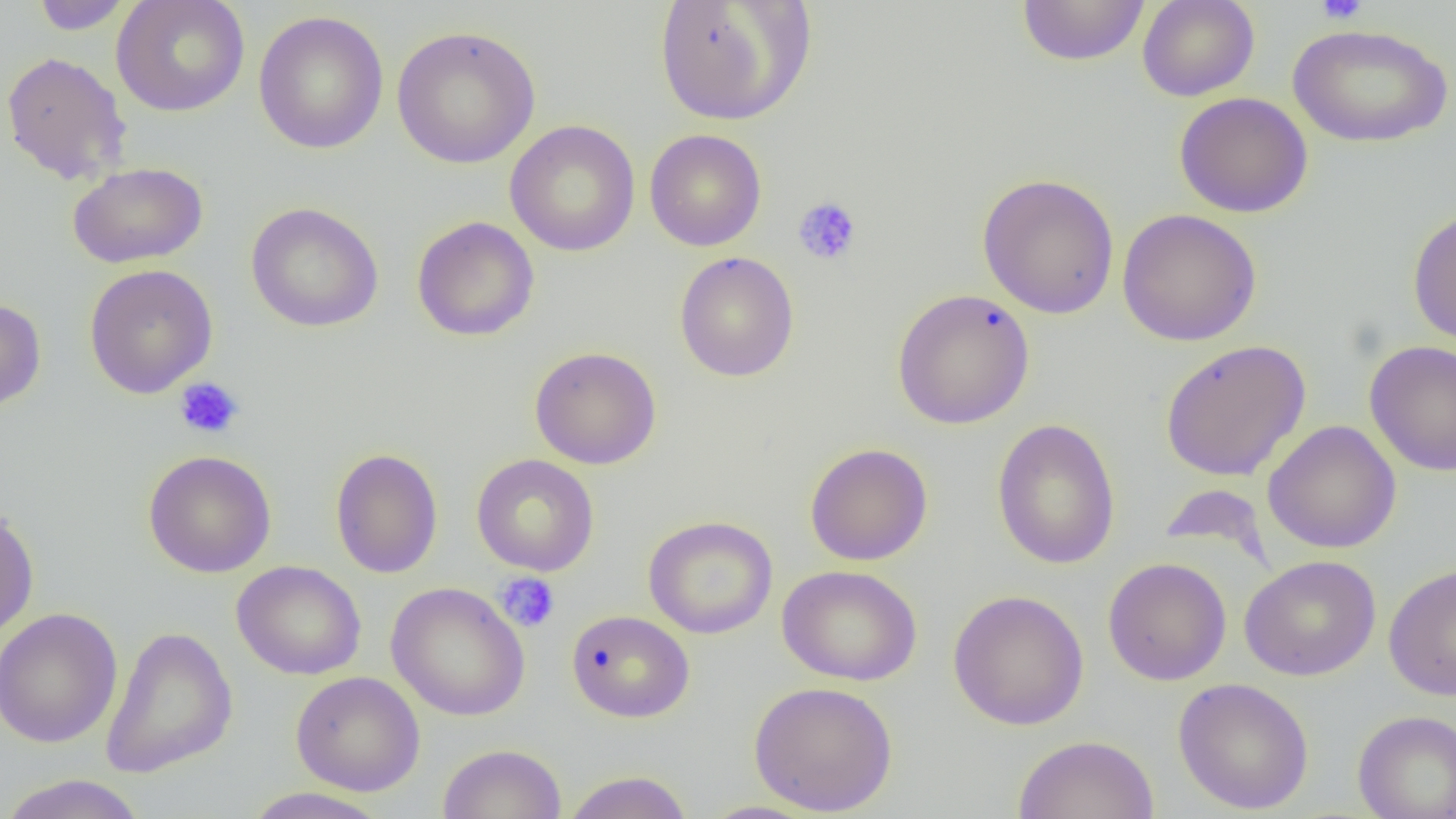

slide-level diagnosis = negative for blood parasites
image size = 1456×819 pixels
platelet locations = approximate bounding boxes as named x1/y1/x2/y2 corners in pixels: (x1=1316, y1=0, x2=1368, y2=25), (x1=793, y1=196, x2=862, y2=265), (x1=174, y1=377, x2=245, y2=440), (x1=495, y1=572, x2=560, y2=633)
uninfected red blood cell locations = approximate bounding boxes as named x1/y1/x2/y2 corners in pixels: (x1=30, y1=0, x2=133, y2=34), (x1=110, y1=0, x2=250, y2=117), (x1=653, y1=0, x2=816, y2=127), (x1=1016, y1=0, x2=1151, y2=67), (x1=1137, y1=0, x2=1259, y2=101), (x1=253, y1=10, x2=389, y2=155), (x1=1287, y1=23, x2=1453, y2=148), (x1=392, y1=25, x2=541, y2=169), (x1=1, y1=51, x2=132, y2=185), (x1=1174, y1=92, x2=1313, y2=218), (x1=505, y1=120, x2=640, y2=257), (x1=644, y1=129, x2=767, y2=252), (x1=68, y1=162, x2=208, y2=269), (x1=977, y1=173, x2=1120, y2=320), (x1=245, y1=202, x2=384, y2=332), (x1=1407, y1=208, x2=1456, y2=346), (x1=1116, y1=209, x2=1262, y2=346), (x1=411, y1=216, x2=540, y2=342), (x1=674, y1=251, x2=799, y2=382), (x1=83, y1=264, x2=218, y2=398), (x1=891, y1=288, x2=1035, y2=429), (x1=0, y1=298, x2=46, y2=413), (x1=1160, y1=339, x2=1312, y2=482), (x1=1364, y1=340, x2=1456, y2=477), (x1=529, y1=346, x2=662, y2=470), (x1=992, y1=418, x2=1121, y2=570), (x1=1263, y1=420, x2=1402, y2=554), (x1=805, y1=442, x2=933, y2=566), (x1=330, y1=447, x2=444, y2=579), (x1=143, y1=449, x2=277, y2=577), (x1=471, y1=454, x2=600, y2=576), (x1=1158, y1=483, x2=1271, y2=561), (x1=0, y1=506, x2=39, y2=641), (x1=643, y1=515, x2=778, y2=639), (x1=1239, y1=555, x2=1381, y2=681), (x1=1102, y1=557, x2=1232, y2=686), (x1=231, y1=560, x2=367, y2=680), (x1=1384, y1=563, x2=1456, y2=701), (x1=777, y1=565, x2=922, y2=686), (x1=386, y1=582, x2=530, y2=721), (x1=947, y1=589, x2=1089, y2=730), (x1=0, y1=608, x2=123, y2=748), (x1=566, y1=609, x2=695, y2=722), (x1=100, y1=625, x2=238, y2=779), (x1=291, y1=671, x2=425, y2=796), (x1=1173, y1=677, x2=1314, y2=814), (x1=747, y1=680, x2=899, y2=816), (x1=1352, y1=709, x2=1456, y2=819), (x1=1013, y1=734, x2=1160, y2=819), (x1=437, y1=743, x2=567, y2=819), (x1=561, y1=770, x2=693, y2=819), (x1=0, y1=773, x2=149, y2=819), (x1=239, y1=787, x2=393, y2=819), (x1=696, y1=800, x2=825, y2=819)
field of view = single
magnification = 1000x
preparation = thin blood smear
modality = light microscopy